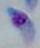
Summary:
  - Magnification: 1000x
  - Identification: Toxoplasma gondii
  - Modality: micrograph